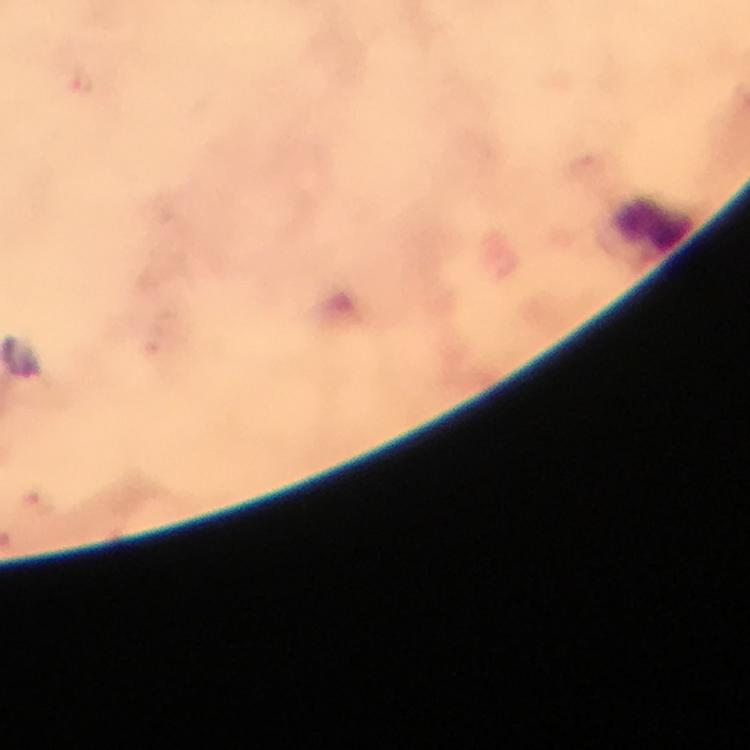

Approximate object centers, in pixels from the top-left corner. Leukocyte locations: (x=652, y=223). Plasmodium parasite locations: (x=78, y=81). Image is 750×750 pixels. Immersion oil applied. A crop from one field of view. Giemsa-stained preparation. Thick blood smear. From a diagnostic examination for malaria. Photographed through the microscope with a smartphone camera. 100x magnification.